Assess the morphology of the red blood cells.
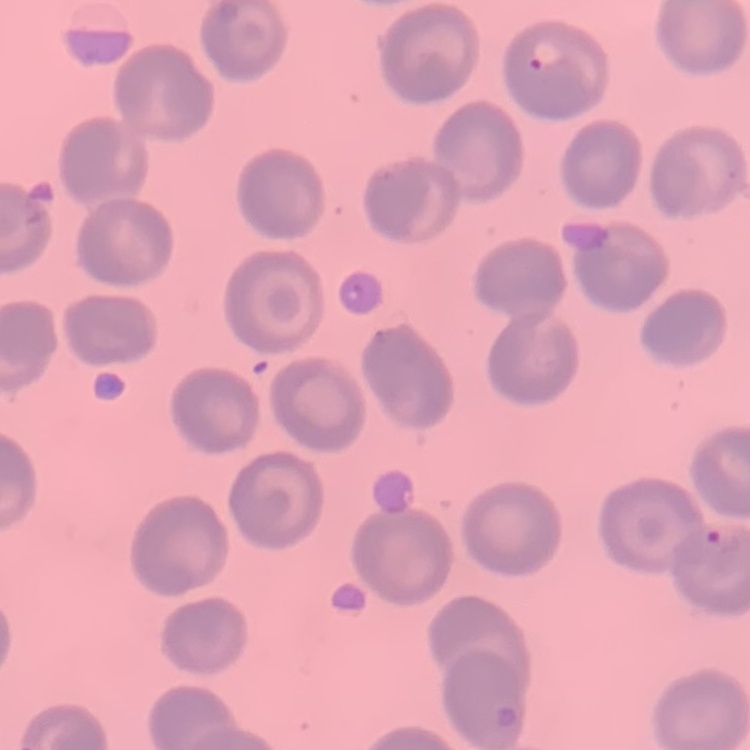
They show no rouleaux formation.

preparation = thin blood smear
image type = one tile cut from a larger photomicrograph
stain = Field's or Giemsa